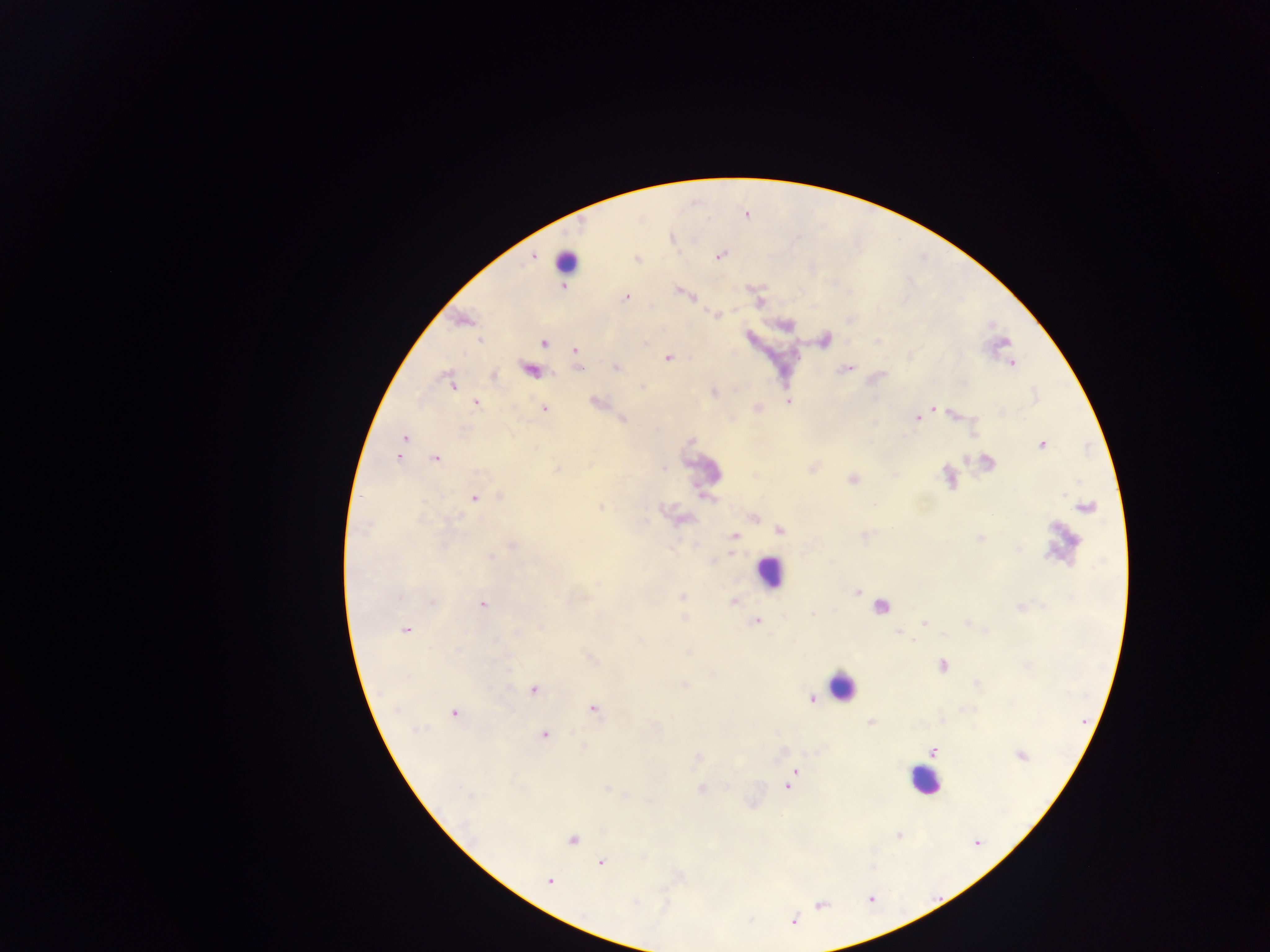

Approximate centers as x y in pixels.
Summary:
  - Plasmodium parasite locations: 720 256; 627 296; 480 340; 544 344; 575 350; 669 358; 1011 362; 615 367; 452 384; 642 386; 477 403; 544 408; 935 408; 915 418; 404 438; 1041 443; 398 457; 435 458; 474 498; 780 530; 865 535; 856 591; 483 605; 814 613; 924 622; 756 623; 406 630; 943 634; 942 665; 533 690; 817 696; 594 708; 455 714; 544 736; 931 752; 796 770; 788 787; 601 862; 549 881; 794 921
  - Leukocyte locations: 569 257; 774 571; 840 686; 926 782
  - Preparation: thick blood smear
  - Capture: mobile-phone photograph through a microscope
  - Field of view: single
  - Image size: 1270×952 pixels
  - Country: Ghana